Report the malaria status of this cell.
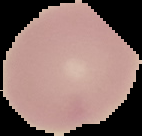
Uninfected.

preparation: thin blood film
image_size: 142×136 pixels
image_type: segmented cell region with the area outside set to black